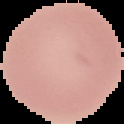

Malaria status: uninfected. Image is 124×124 pixels. From a thin blood film. The area outside the segmented cell region is set to black.